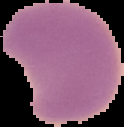

result = Plasmodium parasites identified
image type = cell region segmented out of the field of view; surrounding area masked to black
image size = 124×127 pixels
preparation = thin blood film